Give the extent of all uninfected red blood cells.
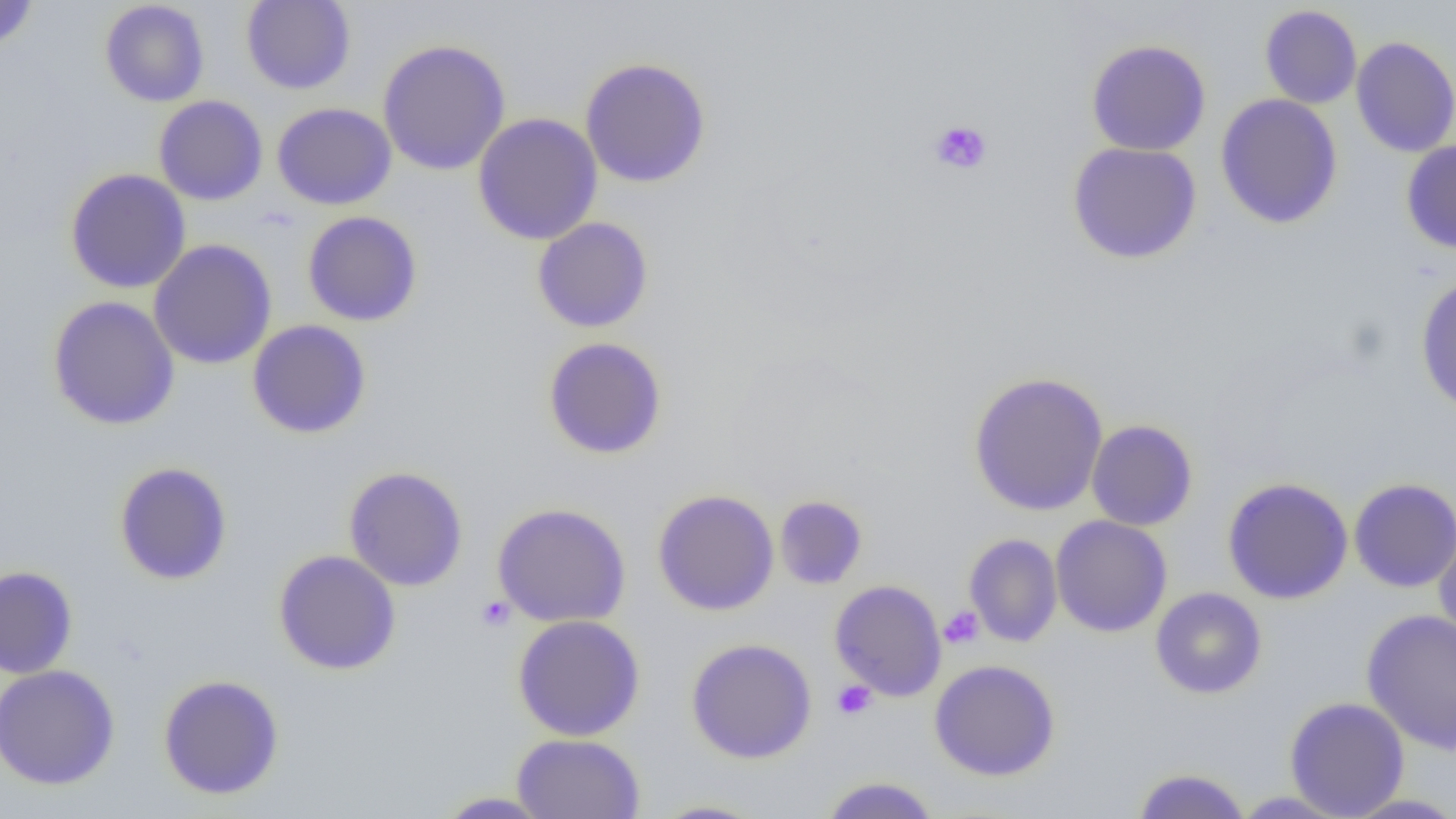
Approximate bounding boxes as [x1, y1, x2, y2] in pixels.
Uninfected red blood cells: [0, 0, 38, 51], [241, 0, 356, 95], [99, 1, 210, 107], [1259, 4, 1362, 109], [1351, 36, 1456, 157], [377, 39, 511, 176], [1086, 39, 1212, 156], [579, 57, 712, 188], [1215, 94, 1343, 230], [154, 95, 268, 206], [272, 102, 397, 210], [472, 113, 603, 245], [1401, 140, 1456, 254], [1067, 141, 1202, 265], [65, 168, 191, 293], [302, 210, 423, 326], [531, 217, 654, 333], [149, 239, 277, 370], [1415, 273, 1456, 415], [47, 296, 180, 431], [247, 319, 372, 439], [543, 337, 667, 459], [968, 371, 1109, 517], [1086, 419, 1198, 531], [114, 461, 233, 585], [343, 466, 469, 591], [1222, 477, 1354, 604], [1349, 477, 1456, 593], [652, 489, 780, 616], [774, 495, 868, 589], [491, 502, 631, 628], [1050, 515, 1173, 637], [1433, 524, 1456, 648], [964, 533, 1063, 647], [273, 549, 401, 675], [0, 566, 78, 679], [829, 579, 947, 701], [1151, 587, 1267, 699], [1361, 609, 1456, 755], [512, 614, 646, 741], [686, 638, 817, 763], [929, 659, 1061, 781], [0, 664, 120, 790], [158, 674, 285, 800], [1284, 696, 1410, 818], [512, 733, 646, 818], [1130, 767, 1253, 818], [818, 776, 942, 818], [433, 791, 556, 818], [1341, 793, 1456, 818], [649, 799, 769, 818].

Summary:
  - Platelet locations: [929, 120, 993, 175], [476, 595, 515, 631], [939, 606, 984, 650], [832, 679, 877, 720]
  - Slide-level diagnosis: negative for blood parasites
  - Field of view: one of a larger specimen
  - Image size: 1456×819 pixels
  - Preparation: thin blood film
  - Modality: optical microscopy
  - Magnification: 1000x